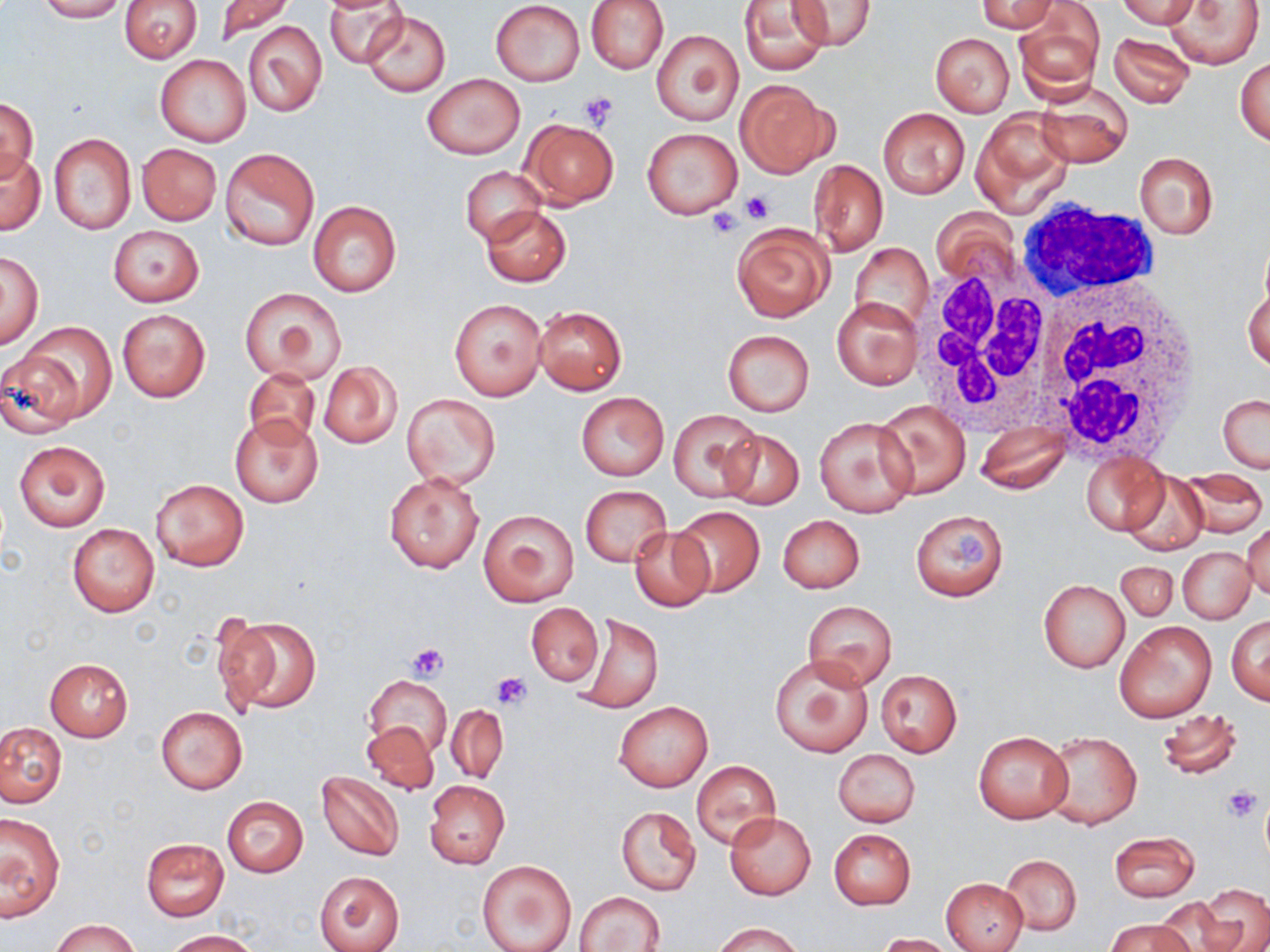

Summary:
  - Coordinate format: approximate bounding boxes as named x1/y1/x2/y2 corners in pixels
  - White blood cell locations: (x1=1015, y1=202, x2=1163, y2=306), (x1=911, y1=257, x2=1065, y2=430), (x1=1029, y1=272, x2=1203, y2=463)
  - Uninfected red blood cell locations: (x1=37, y1=0, x2=126, y2=22), (x1=120, y1=0, x2=201, y2=63), (x1=214, y1=0, x2=294, y2=45), (x1=324, y1=0, x2=412, y2=68), (x1=585, y1=0, x2=669, y2=74), (x1=738, y1=0, x2=831, y2=75), (x1=789, y1=0, x2=875, y2=52), (x1=976, y1=0, x2=1059, y2=33), (x1=1118, y1=0, x2=1201, y2=29), (x1=490, y1=1, x2=585, y2=86), (x1=1164, y1=2, x2=1265, y2=69), (x1=1012, y1=6, x2=1102, y2=102), (x1=360, y1=11, x2=452, y2=97), (x1=242, y1=20, x2=325, y2=117), (x1=652, y1=30, x2=743, y2=126), (x1=1108, y1=32, x2=1195, y2=108), (x1=931, y1=33, x2=1014, y2=116), (x1=155, y1=53, x2=251, y2=147), (x1=1235, y1=56, x2=1269, y2=147), (x1=422, y1=74, x2=524, y2=160), (x1=734, y1=78, x2=835, y2=178), (x1=1034, y1=85, x2=1133, y2=167), (x1=0, y1=97, x2=38, y2=182), (x1=878, y1=108, x2=970, y2=198), (x1=971, y1=109, x2=1073, y2=216), (x1=520, y1=118, x2=619, y2=208), (x1=642, y1=127, x2=744, y2=218), (x1=48, y1=133, x2=137, y2=235), (x1=136, y1=143, x2=221, y2=226), (x1=220, y1=147, x2=320, y2=252), (x1=0, y1=149, x2=44, y2=235), (x1=1134, y1=151, x2=1218, y2=240), (x1=808, y1=159, x2=888, y2=256), (x1=461, y1=167, x2=546, y2=244), (x1=308, y1=201, x2=401, y2=297), (x1=481, y1=206, x2=571, y2=286), (x1=932, y1=206, x2=1022, y2=290), (x1=732, y1=223, x2=832, y2=322), (x1=108, y1=226, x2=203, y2=306), (x1=851, y1=244, x2=933, y2=331), (x1=1, y1=251, x2=43, y2=347), (x1=1243, y1=281, x2=1270, y2=373), (x1=240, y1=287, x2=346, y2=384), (x1=831, y1=296, x2=922, y2=390), (x1=449, y1=299, x2=546, y2=400), (x1=534, y1=305, x2=627, y2=394), (x1=116, y1=307, x2=211, y2=403), (x1=17, y1=322, x2=117, y2=425), (x1=722, y1=330, x2=814, y2=416), (x1=0, y1=353, x2=86, y2=438), (x1=319, y1=362, x2=401, y2=448), (x1=242, y1=368, x2=321, y2=451), (x1=576, y1=392, x2=669, y2=481), (x1=402, y1=393, x2=501, y2=489), (x1=1218, y1=394, x2=1269, y2=474), (x1=874, y1=400, x2=970, y2=499), (x1=669, y1=408, x2=762, y2=501), (x1=229, y1=414, x2=325, y2=508), (x1=814, y1=415, x2=918, y2=517), (x1=975, y1=423, x2=1070, y2=495), (x1=719, y1=429, x2=804, y2=510), (x1=13, y1=439, x2=111, y2=534), (x1=1082, y1=451, x2=1169, y2=534), (x1=1179, y1=469, x2=1267, y2=537), (x1=384, y1=470, x2=486, y2=573), (x1=1120, y1=474, x2=1209, y2=552), (x1=150, y1=479, x2=248, y2=570), (x1=579, y1=485, x2=669, y2=566), (x1=671, y1=505, x2=764, y2=598), (x1=478, y1=509, x2=579, y2=606), (x1=910, y1=510, x2=1010, y2=602), (x1=778, y1=515, x2=865, y2=594), (x1=1243, y1=522, x2=1270, y2=600), (x1=67, y1=524, x2=159, y2=616), (x1=629, y1=527, x2=714, y2=611), (x1=1179, y1=547, x2=1255, y2=624), (x1=1116, y1=561, x2=1178, y2=621), (x1=1037, y1=579, x2=1130, y2=673), (x1=802, y1=600, x2=897, y2=690), (x1=526, y1=603, x2=603, y2=686), (x1=573, y1=612, x2=663, y2=714), (x1=216, y1=614, x2=320, y2=715), (x1=1227, y1=615, x2=1269, y2=704), (x1=1114, y1=620, x2=1218, y2=723), (x1=769, y1=655, x2=874, y2=758), (x1=45, y1=659, x2=133, y2=741), (x1=876, y1=670, x2=962, y2=756), (x1=364, y1=675, x2=452, y2=759), (x1=614, y1=702, x2=712, y2=791), (x1=446, y1=704, x2=509, y2=785), (x1=155, y1=706, x2=248, y2=794), (x1=1156, y1=707, x2=1243, y2=783), (x1=361, y1=721, x2=438, y2=794), (x1=0, y1=722, x2=65, y2=807), (x1=972, y1=731, x2=1074, y2=824), (x1=1044, y1=731, x2=1141, y2=830), (x1=832, y1=748, x2=919, y2=828), (x1=691, y1=760, x2=782, y2=851), (x1=316, y1=770, x2=405, y2=862), (x1=424, y1=780, x2=510, y2=868), (x1=222, y1=796, x2=309, y2=877), (x1=614, y1=805, x2=703, y2=897), (x1=0, y1=813, x2=64, y2=920), (x1=725, y1=813, x2=817, y2=899), (x1=828, y1=828, x2=917, y2=910), (x1=1108, y1=831, x2=1200, y2=902), (x1=140, y1=837, x2=231, y2=921), (x1=1001, y1=854, x2=1082, y2=934), (x1=478, y1=859, x2=576, y2=952), (x1=315, y1=870, x2=405, y2=952), (x1=942, y1=878, x2=1028, y2=951), (x1=1198, y1=884, x2=1270, y2=952), (x1=576, y1=891, x2=665, y2=952), (x1=1148, y1=901, x2=1236, y2=952), (x1=51, y1=919, x2=140, y2=952), (x1=1106, y1=919, x2=1193, y2=952), (x1=714, y1=921, x2=804, y2=952), (x1=164, y1=930, x2=260, y2=951), (x1=872, y1=933, x2=958, y2=952)
  - Platelet locations: (x1=580, y1=91, x2=619, y2=130), (x1=742, y1=191, x2=775, y2=224), (x1=716, y1=198, x2=761, y2=228), (x1=708, y1=208, x2=745, y2=239), (x1=406, y1=641, x2=448, y2=681), (x1=492, y1=673, x2=531, y2=710), (x1=1222, y1=785, x2=1263, y2=823)
  - Slide-level diagnosis: no evidence of blood parasites
  - Magnification: 1000x
  - Preparation: thin blood smear
  - Modality: optical microscopy
  - Field of view: single
  - Stain: May-Grünwald-Giemsa
  - Image size: 1270×952 pixels